Assess this cell for malaria.
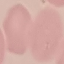

It is uninfected.

Summary:
  - Capture: smartphone through the microscope eyepiece
  - Preparation: thin smear
  - Image type: automatically extracted cell patch, resized to 64 × 64 pixels
  - Stain: Giemsa